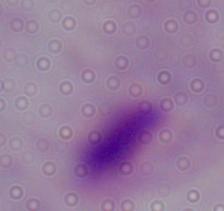
modality: photomicrograph
identification: trichomonad
magnification: 1000x